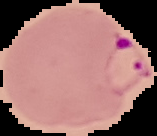
The area outside the segmented cell region is set to black. Image is 157×136 pixels. From a thin blood smear. Malaria status: parasitized.